Report the malaria status of this cell.
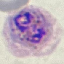

It is parasitized.

capture: smartphone camera at the microscope eyepiece
image_type: cell patch, automatically extracted from a larger field of view and resized to 64 × 64 pixels
stain: Giemsa
preparation: thin blood smear